Describe the morphology of the red blood cells.
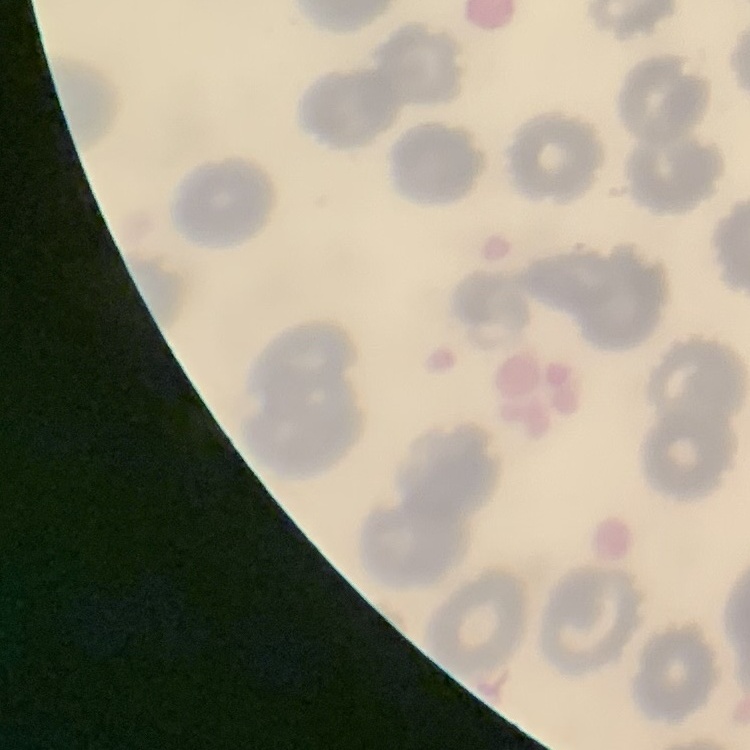

They show no rouleaux formation.

Summary:
  - Stain: Field's or Giemsa
  - Preparation: thin peripheral smear
  - Image type: one tile cut from a larger photomicrograph